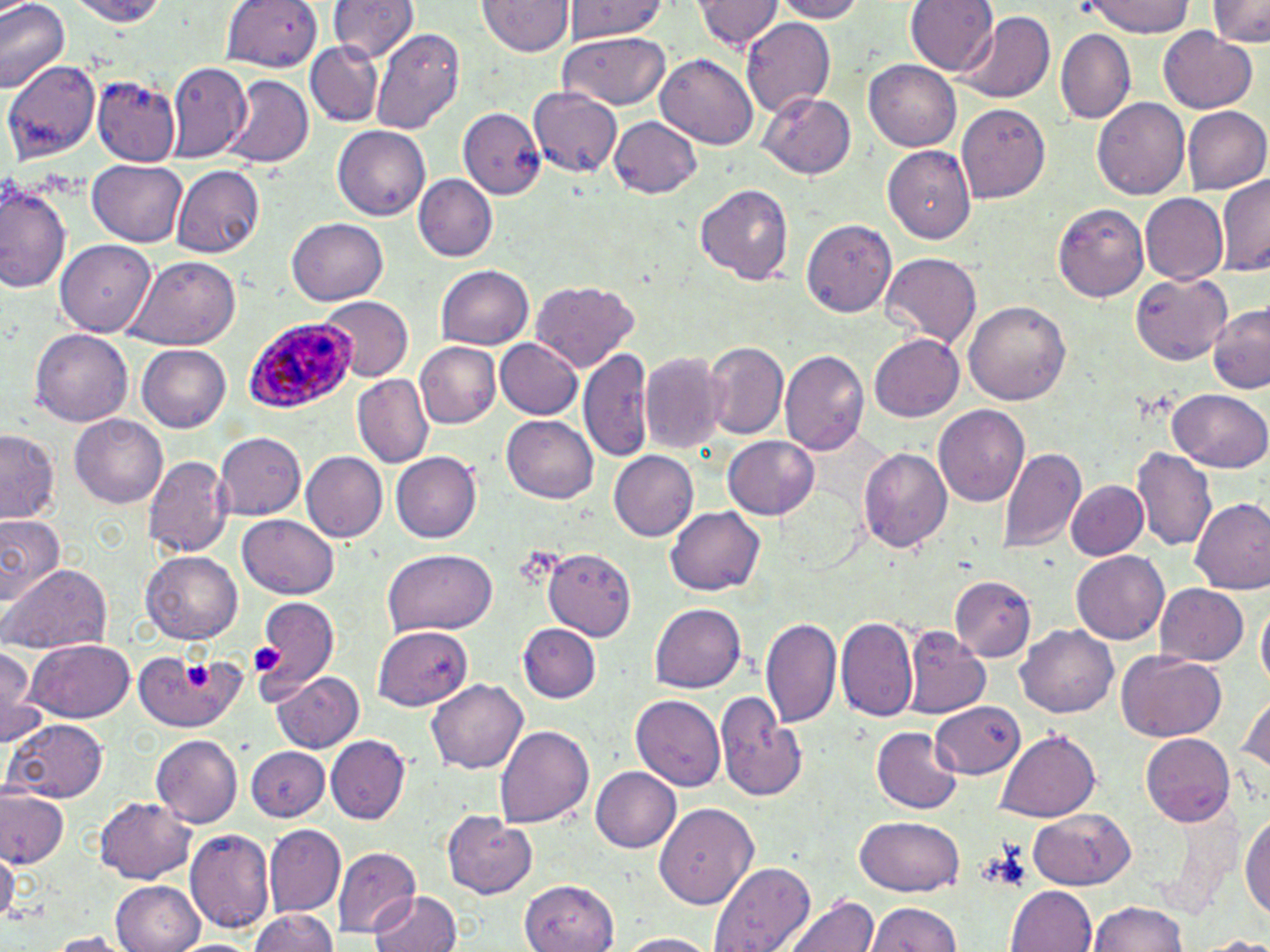
Approximate bounding boxes as (x1,y1)-(x2,y2) corner pairs in pixels. Platelet locations: (249,643)-(281,675), (180,662)-(214,688). Uninfected red blood cell locations: (0,0)-(68,95), (60,0)-(176,25), (695,0)-(781,55), (768,0)-(868,22), (907,0)-(998,80), (1085,0)-(1196,39), (1211,0)-(1268,49), (479,1)-(573,58), (561,1)-(673,44), (223,2)-(323,72), (328,2)-(417,63), (953,15)-(1054,103), (742,17)-(834,116), (370,28)-(464,135), (1158,28)-(1258,114), (1057,30)-(1136,121), (557,33)-(671,110), (307,44)-(382,126), (656,53)-(757,151), (864,59)-(962,152), (5,60)-(101,163), (167,64)-(252,162), (95,75)-(179,164), (222,76)-(311,168), (528,88)-(622,177), (760,91)-(855,179), (1092,97)-(1191,201), (956,102)-(1052,203), (458,107)-(546,200), (1182,107)-(1268,196), (610,116)-(703,200), (332,127)-(430,220), (882,143)-(977,242), (87,161)-(186,246), (172,165)-(265,258), (1216,172)-(1269,278), (413,175)-(495,263), (0,176)-(71,295), (697,184)-(793,284), (1138,193)-(1227,283), (1055,201)-(1150,298), (289,217)-(388,306), (803,218)-(899,315), (57,240)-(156,336), (880,254)-(982,347), (125,256)-(241,348), (435,264)-(534,348), (1130,271)-(1234,363), (533,279)-(641,372), (321,296)-(414,382), (963,298)-(1072,404), (1207,301)-(1270,394), (31,330)-(135,426), (866,333)-(964,422), (494,338)-(583,420), (702,341)-(788,439), (416,343)-(501,429), (136,345)-(231,433), (580,347)-(656,467), (641,351)-(725,455), (782,353)-(869,458), (352,375)-(433,467), (1170,386)-(1270,473), (933,405)-(1030,508), (70,412)-(168,507), (501,415)-(598,501), (1,430)-(60,521), (215,432)-(305,521), (722,434)-(820,521), (998,445)-(1086,556), (1132,445)-(1217,551), (858,446)-(954,553), (300,451)-(387,544), (610,451)-(698,541), (390,453)-(481,544), (143,455)-(229,559), (1066,478)-(1146,560), (1191,498)-(1270,596), (667,506)-(767,596), (0,513)-(64,611), (237,516)-(339,599), (380,549)-(497,635), (545,549)-(636,638), (139,551)-(243,645), (1072,551)-(1168,645), (0,564)-(112,652), (949,575)-(1034,660), (1153,582)-(1250,665), (250,597)-(340,697), (1254,602)-(1269,697), (649,603)-(747,693), (762,615)-(843,730), (836,616)-(917,721), (519,625)-(601,705), (1017,625)-(1118,718), (373,626)-(474,712), (904,629)-(989,718), (26,641)-(134,722), (0,642)-(39,744), (135,649)-(244,732), (1114,651)-(1228,743), (269,671)-(365,753), (424,679)-(529,775), (1239,689)-(1269,785), (716,693)-(806,802), (628,695)-(726,790), (930,702)-(1025,780), (6,718)-(109,804), (495,724)-(595,828), (872,726)-(963,814), (997,731)-(1099,820), (151,734)-(241,827), (1140,734)-(1236,826), (328,737)-(408,823), (247,744)-(329,823), (591,768)-(681,852), (0,789)-(68,871), (95,797)-(196,882), (655,802)-(758,909), (1028,807)-(1137,887), (1242,809)-(1270,922), (442,811)-(535,899), (856,815)-(965,895), (265,826)-(346,915), (185,830)-(274,936), (332,846)-(421,936), (0,849)-(18,925), (710,861)-(816,952), (110,880)-(205,952), (518,881)-(620,952), (1008,886)-(1098,952), (369,890)-(465,952), (788,893)-(878,952), (1088,899)-(1190,952), (868,902)-(963,952), (247,908)-(341,952), (42,932)-(133,951), (614,932)-(720,952), (1191,934)-(1270,951). Plasmodium ovale-infected red blood cell locations: (246,316)-(359,411). Slide-level diagnosis: Plasmodium ovale. Optical microscopy. Image is 1270×952 pixels. Thin blood smear. One field of a larger specimen. 1000x magnification. May-Grünwald-Giemsa stain.